State which parasite is depicted.
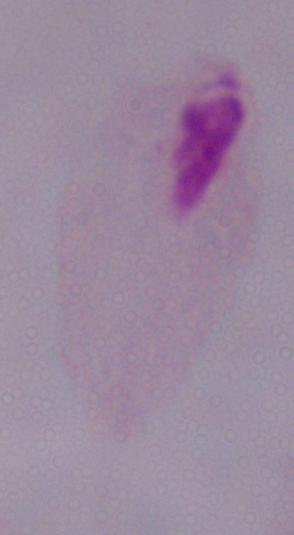

This is a trichomonad.

modality = micrograph
magnification = 1000x